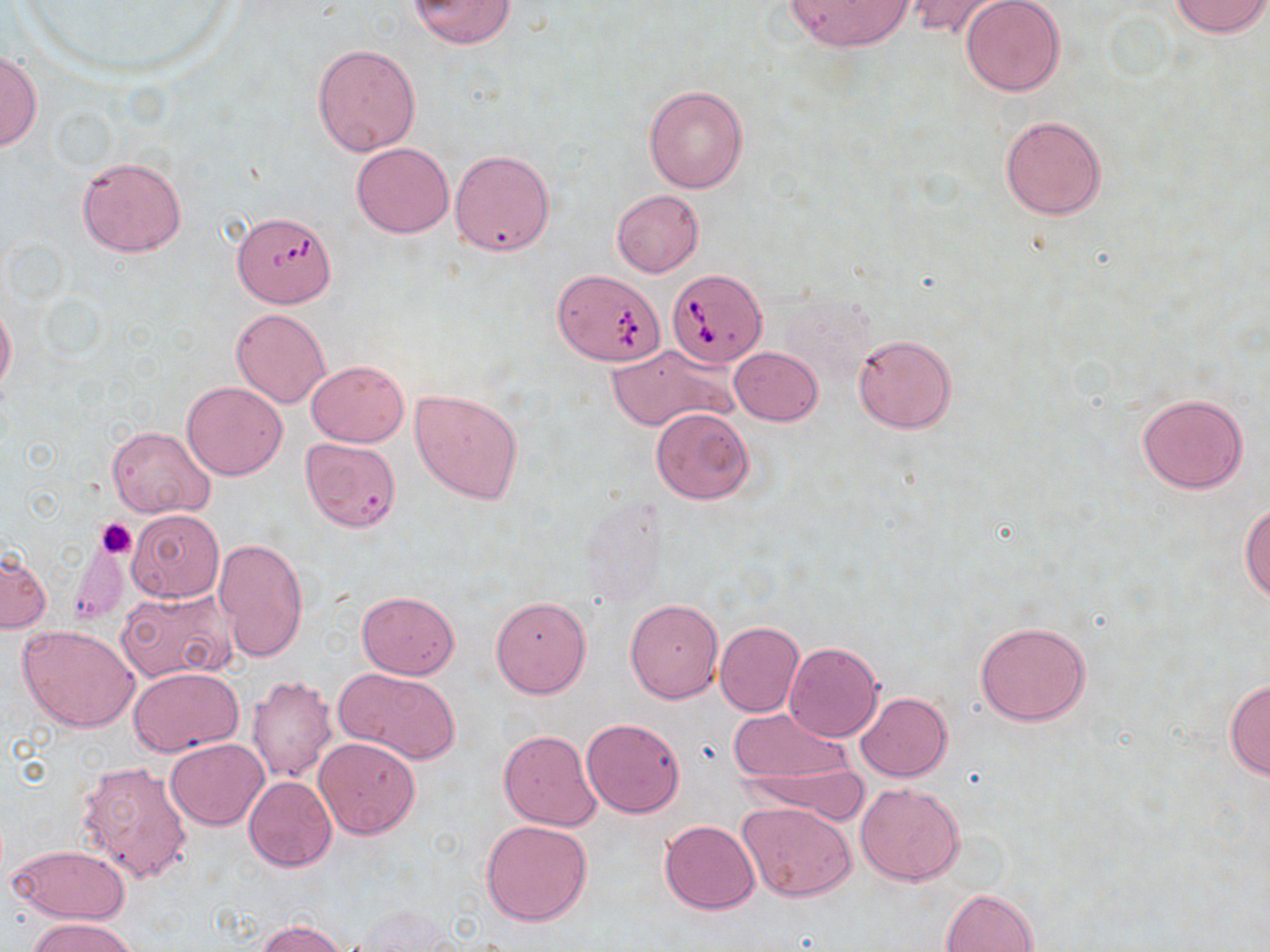

slide-level diagnosis = Babesia divergens
image size = 1270×952 pixels
stain = May-Grünwald-Giemsa
preparation = thin blood smear
modality = optical microscopy
Babesia divergens-infected red blood cell locations = approximate bounding boxes as [x1, y1, x2, y2] in pixels: [667, 267, 767, 368]
field of view = one of a larger specimen
platelet locations = approximate bounding boxes as [x1, y1, x2, y2] in pixels: [96, 517, 136, 557]
uninfected red blood cell locations = approximate bounding boxes as [x1, y1, x2, y2] in pixels: [406, 0, 518, 48], [784, 0, 914, 51], [905, 0, 1014, 42], [1169, 0, 1269, 38], [960, 1, 1064, 97], [313, 43, 420, 155], [0, 51, 41, 151], [643, 84, 748, 193], [998, 114, 1109, 221], [352, 142, 454, 238], [450, 149, 554, 256], [77, 156, 186, 257], [611, 190, 704, 277], [226, 216, 342, 311], [546, 269, 665, 370], [0, 301, 16, 395], [231, 308, 330, 409], [853, 333, 957, 433], [607, 343, 736, 434], [729, 346, 824, 425], [306, 359, 408, 447], [181, 381, 288, 480], [410, 388, 524, 504], [1137, 393, 1249, 493], [650, 407, 755, 505], [107, 426, 214, 518], [300, 437, 401, 534], [1240, 501, 1269, 603], [128, 509, 223, 603], [213, 537, 308, 664], [68, 545, 127, 625], [1, 549, 51, 633], [116, 589, 237, 684], [357, 591, 460, 678], [491, 596, 591, 698], [625, 598, 723, 703], [715, 620, 806, 718], [975, 620, 1091, 726], [17, 624, 141, 732], [783, 642, 882, 742], [129, 665, 244, 756], [336, 668, 462, 765], [247, 674, 338, 783], [1224, 679, 1270, 782], [855, 691, 952, 782], [727, 706, 856, 792], [581, 717, 686, 818], [498, 729, 601, 831], [314, 737, 422, 840], [166, 738, 268, 831], [733, 751, 869, 822], [77, 758, 193, 884], [243, 775, 337, 871], [855, 783, 965, 886], [738, 802, 857, 902], [480, 819, 593, 926], [658, 820, 759, 915], [8, 844, 131, 925], [941, 888, 1039, 952], [354, 905, 453, 952], [28, 918, 139, 952], [257, 919, 348, 952]
magnification = 1000x